Name the blood parasite species.
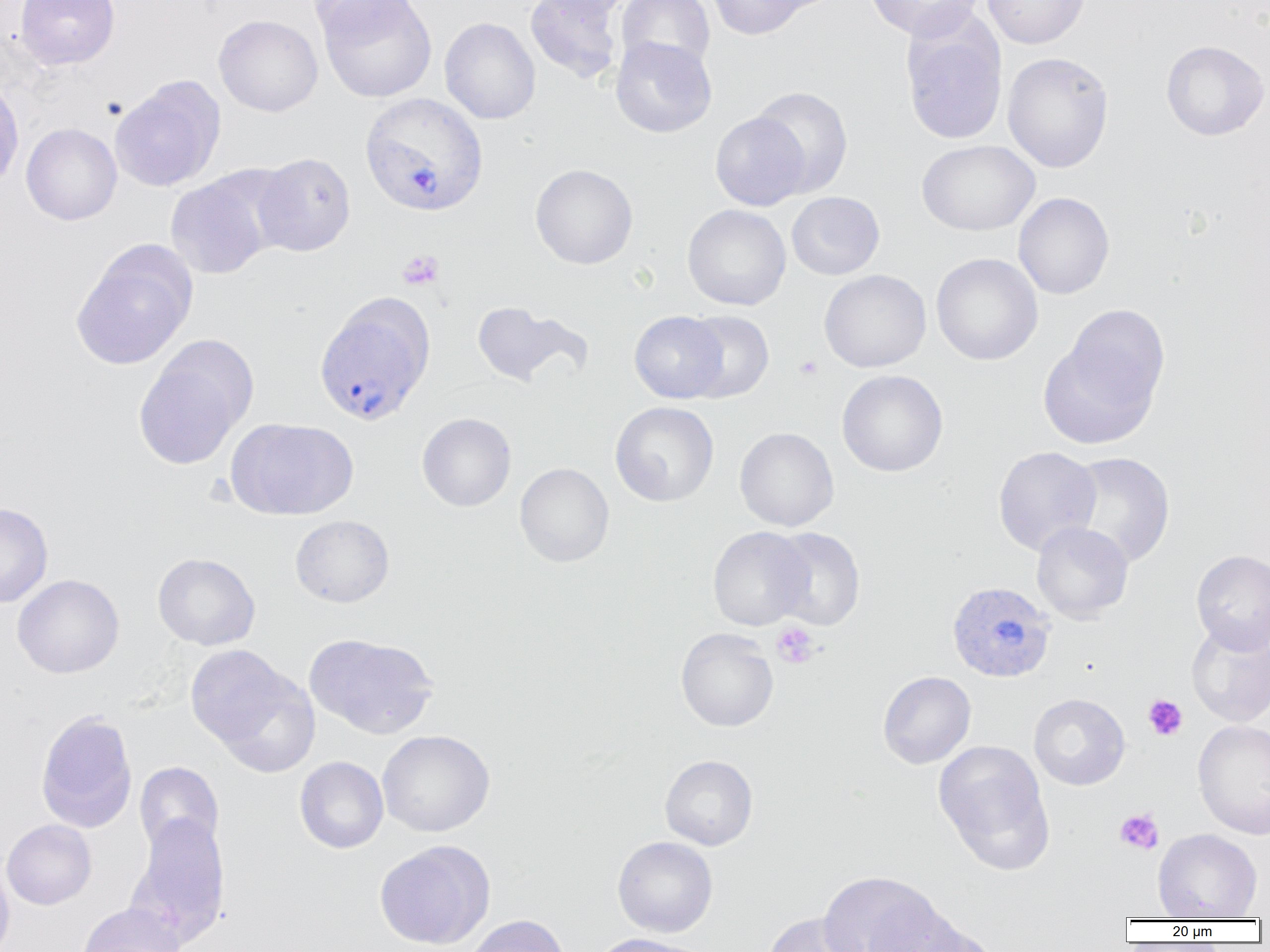

Plasmodium vivax.

Approximate bounding boxes as named x1/y1/x2/y2 corners in pixels. Plasmodium vivax-infected red blood cell locations: (x1=359, y1=92, x2=489, y2=217), (x1=314, y1=299, x2=434, y2=427), (x1=946, y1=580, x2=1056, y2=684). Uninfected red blood cell locations: (x1=15, y1=0, x2=120, y2=69), (x1=307, y1=0, x2=417, y2=40), (x1=317, y1=0, x2=437, y2=103), (x1=525, y1=0, x2=624, y2=83), (x1=533, y1=0, x2=635, y2=20), (x1=616, y1=0, x2=715, y2=74), (x1=707, y1=0, x2=812, y2=39), (x1=864, y1=0, x2=983, y2=41), (x1=982, y1=0, x2=1090, y2=49), (x1=214, y1=14, x2=323, y2=117), (x1=439, y1=17, x2=541, y2=124), (x1=901, y1=18, x2=1007, y2=145), (x1=610, y1=36, x2=717, y2=138), (x1=1161, y1=40, x2=1269, y2=141), (x1=1002, y1=51, x2=1114, y2=173), (x1=0, y1=77, x2=24, y2=191), (x1=110, y1=77, x2=225, y2=192), (x1=749, y1=85, x2=854, y2=197), (x1=710, y1=111, x2=810, y2=211), (x1=21, y1=122, x2=122, y2=225), (x1=917, y1=139, x2=1040, y2=235), (x1=252, y1=152, x2=356, y2=257), (x1=530, y1=163, x2=638, y2=269), (x1=165, y1=172, x2=278, y2=280), (x1=787, y1=191, x2=885, y2=280), (x1=1013, y1=192, x2=1114, y2=300), (x1=682, y1=204, x2=791, y2=310), (x1=71, y1=244, x2=196, y2=370), (x1=931, y1=253, x2=1043, y2=366), (x1=819, y1=269, x2=931, y2=372), (x1=470, y1=300, x2=591, y2=389), (x1=1043, y1=309, x2=1169, y2=447), (x1=629, y1=311, x2=729, y2=403), (x1=681, y1=311, x2=774, y2=403), (x1=133, y1=345, x2=252, y2=469), (x1=836, y1=369, x2=948, y2=477), (x1=610, y1=402, x2=719, y2=506), (x1=417, y1=412, x2=516, y2=512), (x1=226, y1=417, x2=358, y2=521), (x1=735, y1=427, x2=839, y2=531), (x1=993, y1=446, x2=1101, y2=556), (x1=1063, y1=452, x2=1176, y2=568), (x1=514, y1=462, x2=614, y2=567), (x1=0, y1=502, x2=53, y2=608), (x1=290, y1=515, x2=395, y2=607), (x1=1031, y1=521, x2=1134, y2=624), (x1=707, y1=526, x2=812, y2=631), (x1=768, y1=527, x2=866, y2=630), (x1=1191, y1=549, x2=1270, y2=653), (x1=152, y1=553, x2=260, y2=650), (x1=12, y1=574, x2=124, y2=678), (x1=1186, y1=621, x2=1270, y2=727), (x1=675, y1=628, x2=779, y2=732), (x1=304, y1=633, x2=439, y2=739), (x1=186, y1=644, x2=316, y2=767), (x1=877, y1=670, x2=976, y2=769), (x1=1029, y1=693, x2=1130, y2=791), (x1=35, y1=710, x2=138, y2=833), (x1=1192, y1=719, x2=1270, y2=840), (x1=377, y1=729, x2=495, y2=837), (x1=933, y1=739, x2=1055, y2=874), (x1=659, y1=754, x2=759, y2=850), (x1=295, y1=756, x2=389, y2=854), (x1=135, y1=762, x2=224, y2=858), (x1=127, y1=814, x2=231, y2=948), (x1=1, y1=819, x2=97, y2=910), (x1=1152, y1=828, x2=1262, y2=920), (x1=612, y1=835, x2=718, y2=937), (x1=374, y1=840, x2=495, y2=949), (x1=0, y1=856, x2=15, y2=952), (x1=818, y1=871, x2=944, y2=952), (x1=77, y1=902, x2=186, y2=952), (x1=868, y1=904, x2=990, y2=951), (x1=762, y1=912, x2=867, y2=952), (x1=464, y1=914, x2=569, y2=952), (x1=591, y1=933, x2=709, y2=952). Platelet locations: (x1=397, y1=249, x2=444, y2=290), (x1=794, y1=356, x2=823, y2=381), (x1=771, y1=622, x2=819, y2=668), (x1=1143, y1=695, x2=1188, y2=741), (x1=1114, y1=809, x2=1164, y2=855). Single field of view. Thin blood smear. Captured at 1000x magnification. Light microscopy. Image is 1270×952 pixels.